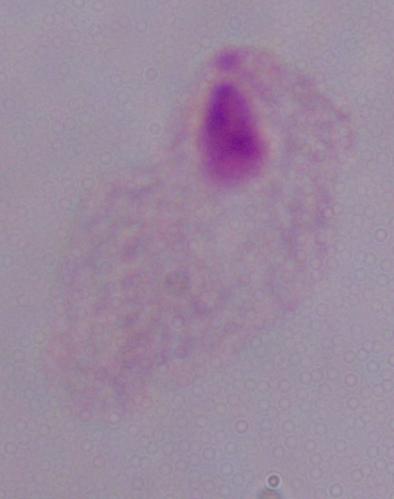

modality = micrograph
identification = trichomonad
magnification = 1000x